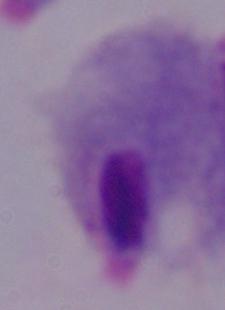

{
  "identification": "trichomonad",
  "modality": "photomicrograph",
  "magnification": "1000x"
}